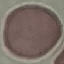
Result: no malaria parasites seen. Giemsa stain. Thin smear of blood. Acquired by smartphone through the microscope eyepiece. Cell patch, automatically extracted from a larger field of view and resized to 64 × 64 pixels.